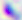
Summary:
  - Identification: Toxoplasma gondii
  - Magnification: 400x
  - Modality: micrograph